Identify the blood parasite species.
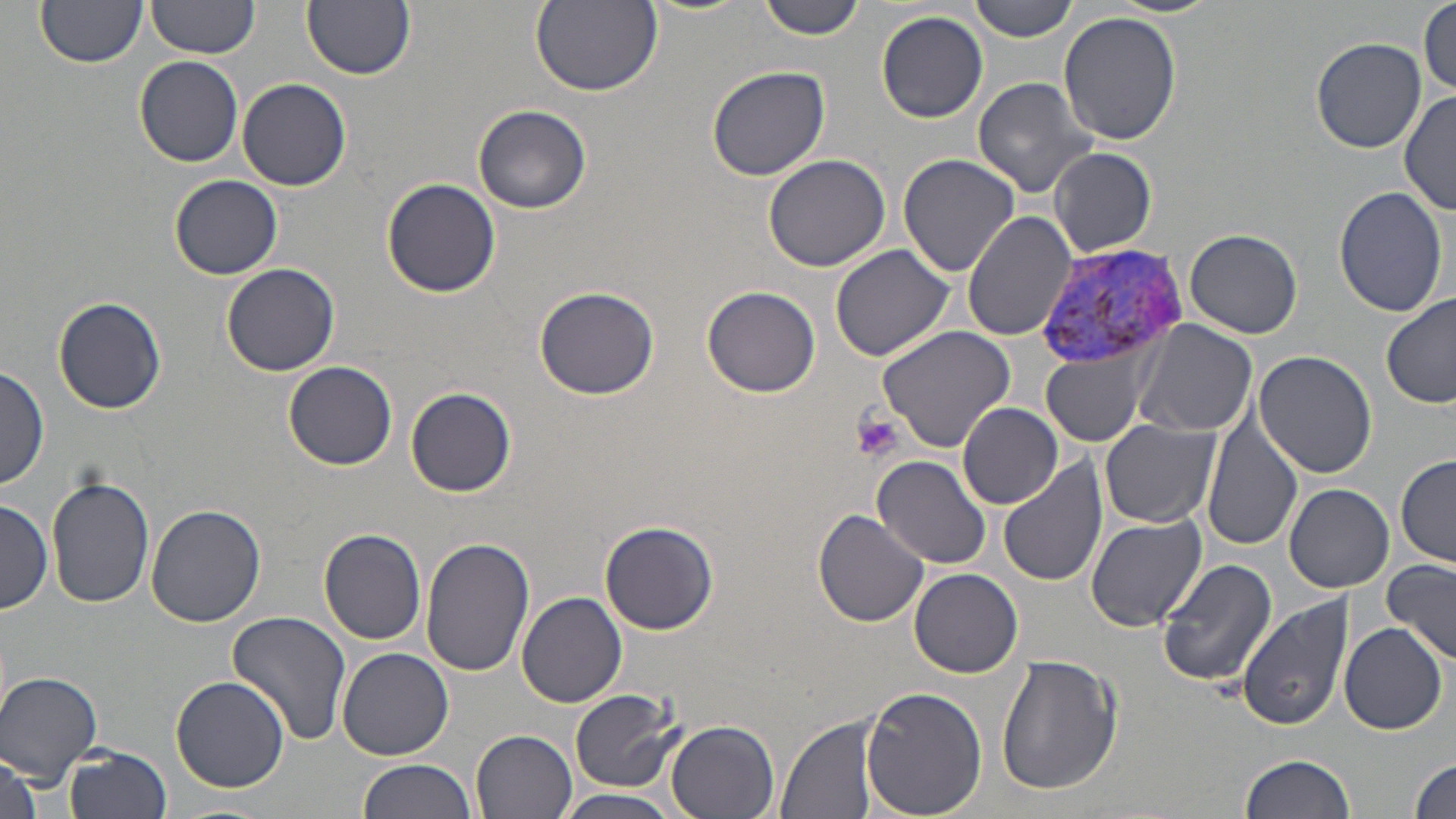
Plasmodium vivax.

Approximate bounding boxes as (x1, y1, x2, y2) in pixels. Uninfected red blood cell locations: (147, 0, 259, 59), (530, 0, 663, 97), (759, 0, 868, 40), (969, 0, 1081, 42), (1112, 0, 1224, 18), (303, 1, 415, 80), (1418, 1, 1455, 98), (38, 2, 146, 69), (877, 10, 988, 123), (1059, 12, 1183, 147), (1310, 37, 1427, 152), (134, 56, 244, 167), (705, 64, 831, 182), (237, 77, 352, 191), (972, 77, 1100, 199), (1400, 89, 1456, 216), (473, 104, 594, 214), (1048, 147, 1156, 255), (897, 152, 1022, 278), (764, 155, 894, 274), (170, 174, 283, 278), (382, 178, 501, 298), (1333, 187, 1449, 318), (962, 211, 1077, 340), (1185, 228, 1302, 339), (830, 244, 955, 361), (221, 263, 340, 376), (702, 285, 821, 397), (533, 287, 660, 400), (1381, 293, 1455, 412), (54, 296, 167, 414), (1132, 319, 1259, 439), (877, 325, 1016, 452), (1042, 349, 1151, 447), (1253, 349, 1379, 479), (282, 361, 398, 469), (0, 364, 50, 490), (405, 386, 517, 498), (959, 403, 1063, 508), (1204, 410, 1304, 553), (1100, 419, 1218, 528), (1396, 455, 1455, 566), (998, 456, 1109, 588), (873, 457, 992, 569), (46, 474, 155, 610), (1284, 484, 1393, 593), (0, 498, 53, 614), (147, 504, 265, 625), (812, 507, 930, 628), (1086, 516, 1206, 632), (600, 521, 719, 635), (318, 527, 427, 646), (421, 534, 536, 678), (1156, 559, 1278, 687), (1384, 559, 1456, 663), (910, 569, 1024, 678), (518, 592, 627, 709), (1238, 595, 1353, 732), (226, 611, 352, 745), (1338, 621, 1446, 735), (338, 646, 455, 759), (996, 654, 1122, 797), (0, 670, 103, 785), (171, 676, 289, 791), (861, 684, 987, 819), (570, 687, 684, 790), (568, 699, 774, 807), (777, 717, 879, 819), (666, 720, 780, 819), (471, 729, 577, 818), (61, 745, 173, 819), (1409, 752, 1456, 819), (1, 753, 45, 819), (1238, 753, 1356, 819), (357, 759, 474, 819), (552, 790, 683, 819). Platelet locations: (850, 411, 903, 463). Plasmodium vivax-infected red blood cell locations: (1035, 243, 1195, 369). May-Grünwald-Giemsa stain. 1000x magnification. Thin blood smear. Image is 1456×819 pixels. One field of a larger specimen. Optical microscopy.